Name the parasite shown.
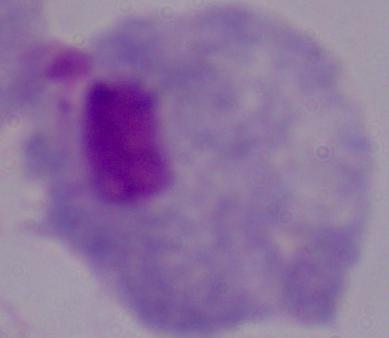
This is a trichomonad.

modality = photomicrograph
magnification = 1000x